Name the cell type shown.
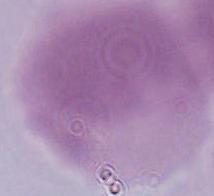
An erythrocyte.

Photomicrograph. 1000x magnification.